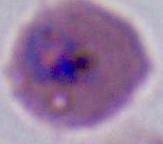

400x or 1000x magnification. Micrograph. A Plasmodium parasite is shown.